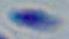
Micrograph. Captured at 1000x magnification. Toxoplasma gondii is seen.